Report the malaria status of this cell.
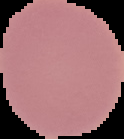
Uninfected.

image_size: 124×139 pixels
preparation: thin blood smear
image_type: segmented cell region with the area outside set to black